Outline each uninfected red blood cell.
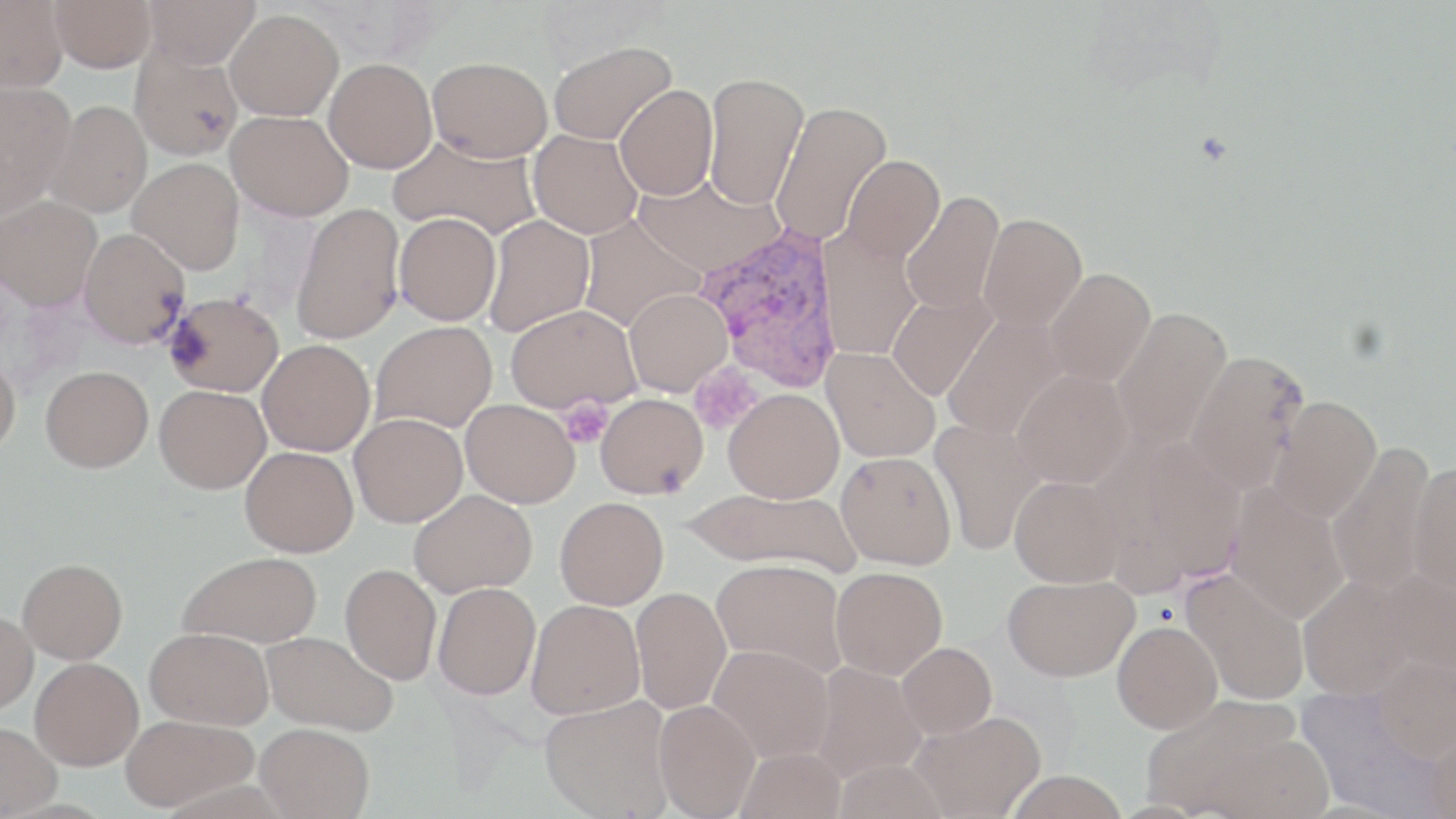

Approximate bounding boxes as (x1,y1)-(x2,y2) corner pairs in pixels.
Uninfected red blood cells: (0,0)-(68,91), (49,0)-(157,72), (141,0)-(259,69), (225,9)-(343,120), (547,41)-(677,145), (130,45)-(244,161), (427,56)-(552,162), (324,58)-(437,173), (703,73)-(807,210), (0,82)-(77,215), (614,84)-(718,200), (44,100)-(153,218), (770,101)-(893,246), (226,110)-(354,221), (528,129)-(642,238), (387,133)-(542,241), (840,155)-(945,264), (128,157)-(244,274), (633,174)-(782,276), (901,191)-(1004,314), (1,196)-(101,310), (291,203)-(405,344), (394,212)-(501,325), (579,213)-(705,332), (979,213)-(1087,331), (484,215)-(594,336), (78,228)-(190,348), (819,231)-(923,359), (1044,268)-(1156,387), (624,289)-(732,396), (164,291)-(284,397), (887,291)-(998,402), (506,304)-(641,412), (1110,306)-(1233,452), (943,314)-(1067,441), (370,321)-(497,433), (258,339)-(376,456), (0,348)-(21,459), (821,348)-(940,462), (1184,350)-(1309,494), (40,365)-(153,472), (1012,368)-(1132,488), (154,385)-(270,494), (724,388)-(844,502), (596,393)-(707,498), (1267,394)-(1382,522), (461,399)-(579,508), (349,413)-(467,527), (930,419)-(1045,556), (1113,437)-(1247,587), (1326,442)-(1438,594), (240,446)-(358,557), (836,451)-(956,569), (1408,460)-(1456,599), (1010,475)-(1126,587), (1225,484)-(1349,624), (682,487)-(860,574), (409,489)-(537,597), (555,497)-(668,609), (178,551)-(322,649), (17,558)-(127,664), (712,559)-(846,677), (340,564)-(441,684), (1374,565)-(1456,680), (831,566)-(947,678), (1181,569)-(1310,705), (1297,573)-(1423,700), (1002,574)-(1138,681), (433,582)-(541,700), (631,587)-(731,715), (526,599)-(644,719), (0,611)-(38,714), (1112,621)-(1223,733), (145,627)-(274,730), (262,630)-(398,736), (897,642)-(996,738), (708,645)-(834,763), (1370,654)-(1456,762), (30,657)-(143,769), (809,662)-(925,782), (1140,694)-(1309,816), (540,695)-(674,818), (653,700)-(760,819), (909,710)-(1046,818), (120,714)-(257,812), (255,722)-(374,818), (0,723)-(60,818), (1425,723)-(1456,819), (736,746)-(847,819), (1003,770)-(1130,819).

Plasmodium vivax-infected red blood cell locations: (693,220)-(845,395). Platelet locations: (557,397)-(612,449). Slide-level diagnosis: Plasmodium vivax. Thin blood smear. Image is 1456×819 pixels. Single field of view. Optical microscopy. Captured at 1000x magnification. May-Grünwald-Giemsa stain.